Report the malaria status of this cell.
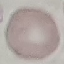

It is uninfected.

Summary:
  - Preparation: thin blood smear
  - Stain: Giemsa
  - Capture: smartphone camera at the microscope eyepiece
  - Image type: automatically extracted cell patch, resized to 64 × 64 pixels